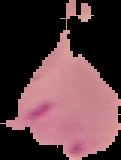
Summary:
  - Result: Plasmodium parasites detected
  - Preparation: thin blood smear
  - Image type: segmented cell region on a black background
  - Image size: 121×160 pixels